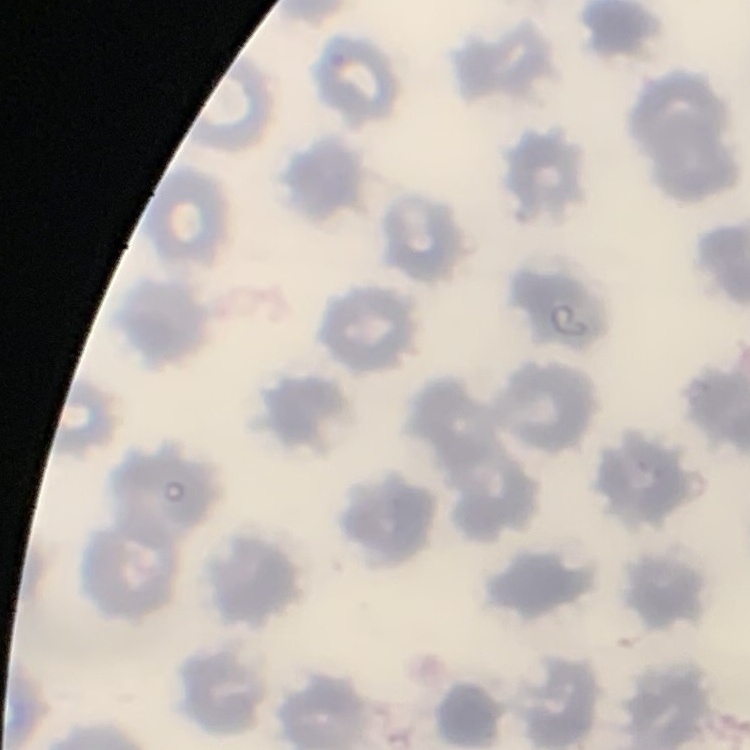

Summary:
  - Red blood cell morphology: no rouleaux formation
  - Stain: Field's or Giemsa
  - Preparation: thin peripheral smear
  - Image type: one tile cut from a larger photomicrograph